Locate and identify every blood parasite.
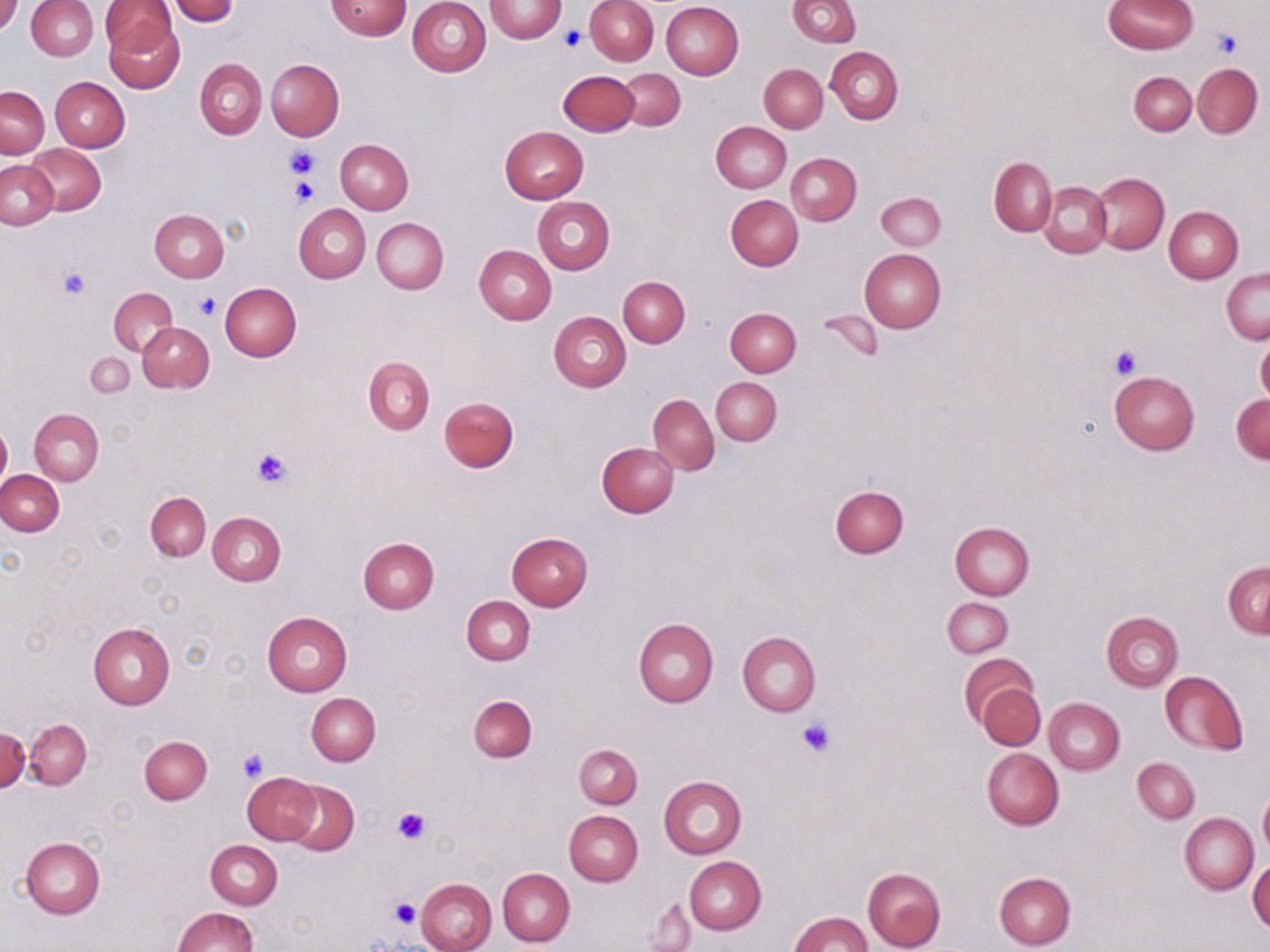
No blood parasites observed.

Summary:
  - Coordinate format: approximate bounding boxes as [x1, y1, x2, y2] in pixels
  - Uninfected red blood cell locations: [0, 0, 24, 35], [98, 0, 176, 56], [407, 0, 492, 76], [485, 0, 567, 43], [586, 0, 659, 65], [786, 0, 860, 47], [26, 1, 98, 59], [170, 1, 238, 24], [325, 1, 411, 40], [1105, 1, 1196, 54], [661, 2, 744, 80], [104, 11, 183, 91], [826, 47, 903, 124], [195, 58, 267, 139], [267, 58, 344, 140], [1193, 62, 1262, 139], [760, 64, 827, 133], [618, 69, 685, 130], [559, 71, 639, 135], [1129, 72, 1196, 135], [50, 77, 129, 152], [42, 78, 118, 214], [1, 86, 49, 158], [711, 122, 791, 193], [500, 126, 588, 204], [336, 140, 414, 215], [28, 144, 105, 215], [786, 152, 861, 225], [989, 156, 1057, 236], [0, 160, 58, 231], [1090, 173, 1168, 252], [1039, 182, 1112, 257], [876, 192, 945, 250], [532, 195, 615, 274], [726, 195, 803, 271], [293, 204, 370, 282], [1164, 206, 1243, 283], [149, 209, 228, 282], [372, 218, 448, 295], [474, 245, 556, 325], [859, 248, 945, 334], [1222, 268, 1269, 344], [618, 276, 690, 347], [220, 282, 301, 362], [108, 287, 179, 357], [725, 308, 801, 377], [819, 309, 883, 362], [550, 312, 631, 392], [137, 321, 214, 392], [1256, 335, 1270, 407], [86, 351, 133, 398], [364, 356, 435, 435], [1109, 370, 1199, 454], [711, 376, 782, 445], [1231, 393, 1270, 464], [649, 395, 719, 475], [440, 396, 520, 472], [30, 408, 104, 486], [0, 422, 11, 493], [598, 443, 680, 517], [0, 470, 65, 536], [830, 484, 909, 558], [146, 493, 210, 561], [208, 511, 286, 586], [949, 522, 1034, 600], [507, 532, 593, 611], [359, 538, 439, 613], [1223, 561, 1270, 638], [462, 596, 534, 666], [943, 598, 1013, 657], [262, 611, 352, 697], [1101, 611, 1183, 691], [634, 618, 718, 707], [88, 621, 175, 709], [737, 632, 821, 716], [960, 653, 1039, 730], [1160, 671, 1248, 754], [976, 682, 1045, 751], [307, 692, 381, 765], [469, 695, 537, 761], [1044, 697, 1125, 774], [25, 719, 92, 789], [1, 727, 30, 793], [140, 736, 212, 805], [574, 744, 642, 808], [981, 748, 1064, 830], [1132, 757, 1200, 822], [243, 772, 320, 844], [659, 776, 746, 859], [286, 781, 358, 855], [1258, 791, 1270, 858], [564, 810, 643, 886], [1180, 813, 1257, 894], [22, 838, 104, 918], [206, 840, 283, 909], [685, 856, 766, 934], [1248, 859, 1270, 934], [863, 867, 946, 952], [497, 868, 575, 947], [995, 872, 1076, 949], [416, 878, 497, 952], [645, 896, 696, 950], [173, 907, 258, 952], [791, 912, 871, 952]
  - Platelet locations: [559, 28, 583, 52], [1211, 30, 1240, 58], [285, 144, 321, 179], [290, 177, 319, 207], [59, 266, 91, 299], [193, 292, 222, 319], [1108, 345, 1142, 380], [251, 446, 292, 489], [797, 717, 838, 759], [236, 746, 271, 782], [392, 807, 429, 844], [388, 896, 422, 928]
  - Slide-level diagnosis: no evidence of blood parasites
  - Preparation: thin blood film
  - Magnification: 1000x
  - Image size: 1270×952 pixels
  - Modality: light microscopy
  - Stain: May-Grünwald-Giemsa
  - Field of view: single